Point out each malaria parasite and classify it by life-cycle stage.
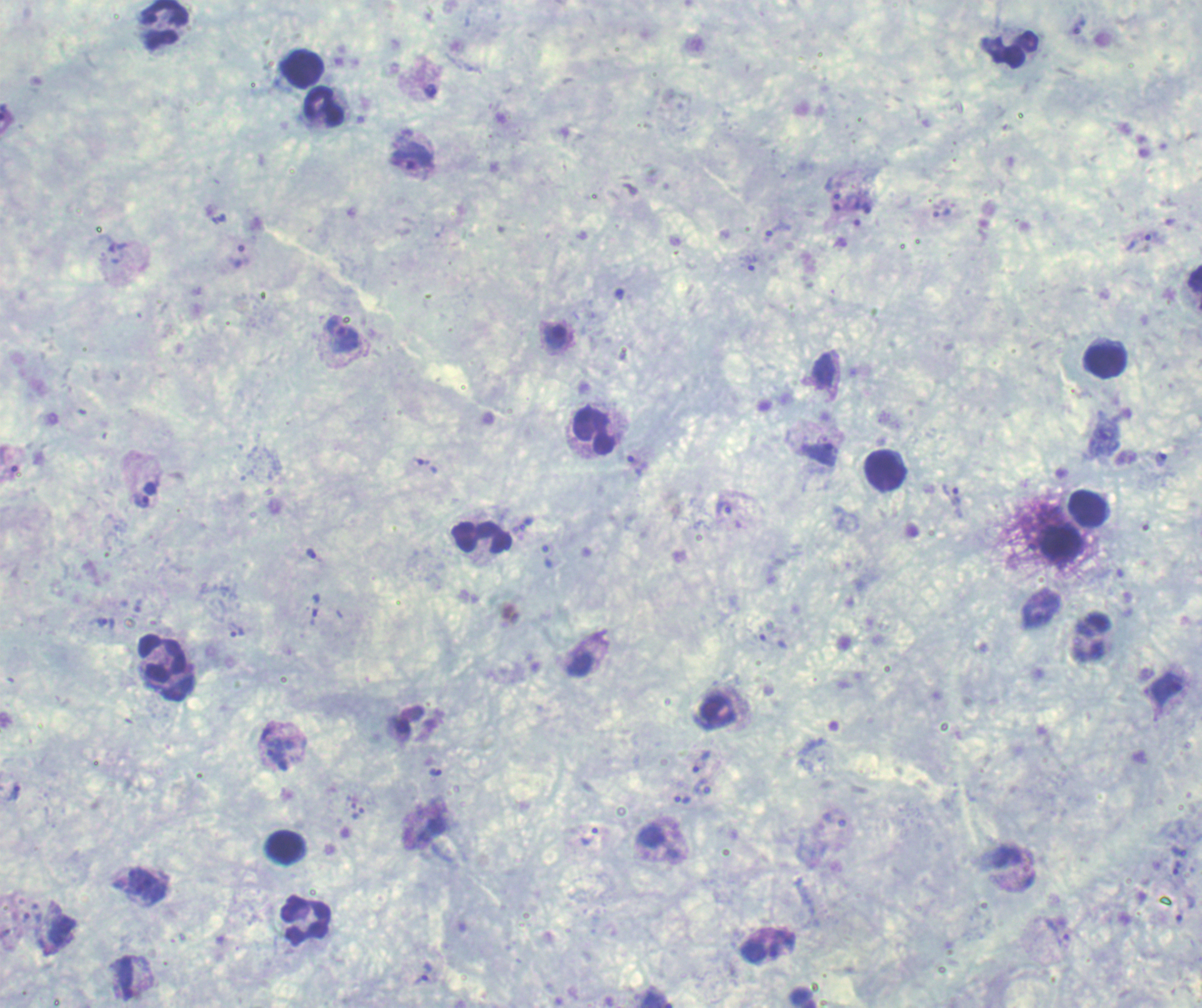
Approximate centers as (x, y) in pixels.
Trophozoites: (431, 90), (412, 156), (832, 188), (862, 204), (941, 213), (777, 230), (1139, 242), (750, 263), (343, 335), (819, 453), (633, 463), (426, 465), (952, 495), (141, 500), (724, 508), (310, 554), (547, 556), (106, 622), (236, 631), (1167, 688), (279, 755), (701, 762), (14, 792), (683, 799), (590, 836), (1179, 852), (1177, 867), (1062, 939), (776, 951), (753, 952), (423, 973).
Gametocytes: (555, 336).
No schizont forms observed.

Approximate centers as (x, y) in pixels. Leukocyte locations: (165, 23), (1008, 48), (300, 68), (322, 106), (1105, 359), (594, 431), (885, 471), (1089, 510), (482, 538), (1091, 638), (165, 667), (285, 847), (304, 920). Single field of view. Previously used in a real diagnosis. 100x magnification. Thick blood film. Background quality: good. Romanowsky-stained preparation. Image is 1202×1008 pixels.